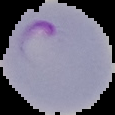 The area outside the segmented cell region is set to black. Malaria status: parasitized. From a thin blood smear. Image is 115×115 pixels.